Classify this cell by malaria status.
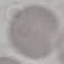

It is uninfected.

stain = Giemsa
capture = smartphone camera at the microscope eyepiece
preparation = thin smear
image type = cell patch, automatically extracted from a larger field of view and resized to 64 × 64 pixels